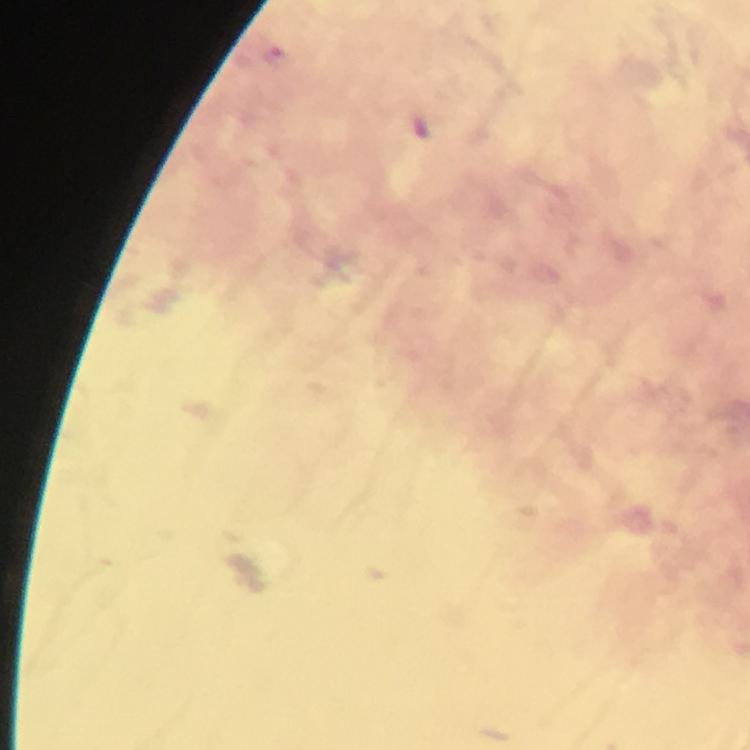

context = from a diagnostic examination for malaria
immersion oil = applied
preparation = thick blood smear
magnification = 100x
capture = smartphone camera through the microscope
image size = 750×750 pixels
stain = Giemsa
cropped from = a single field of view
Plasmodium parasite locations = approximate centers as [x, y] in pixels: [274, 55]